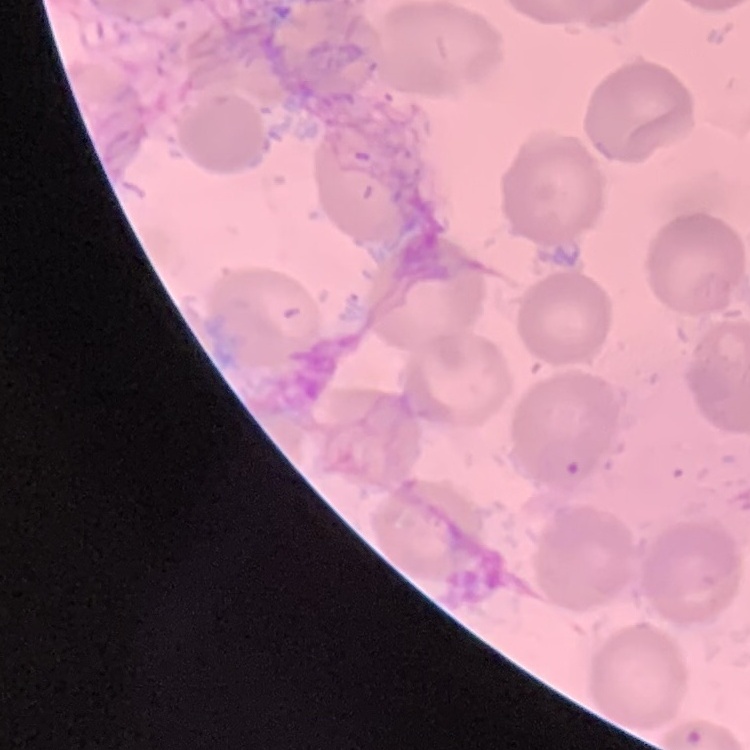

The erythrocytes exhibit no rouleaux formation. Stained with either Field's or Giemsa. Thin peripheral smear. Square crop of a larger photomicrograph.